Describe the morphology of the erythrocytes.
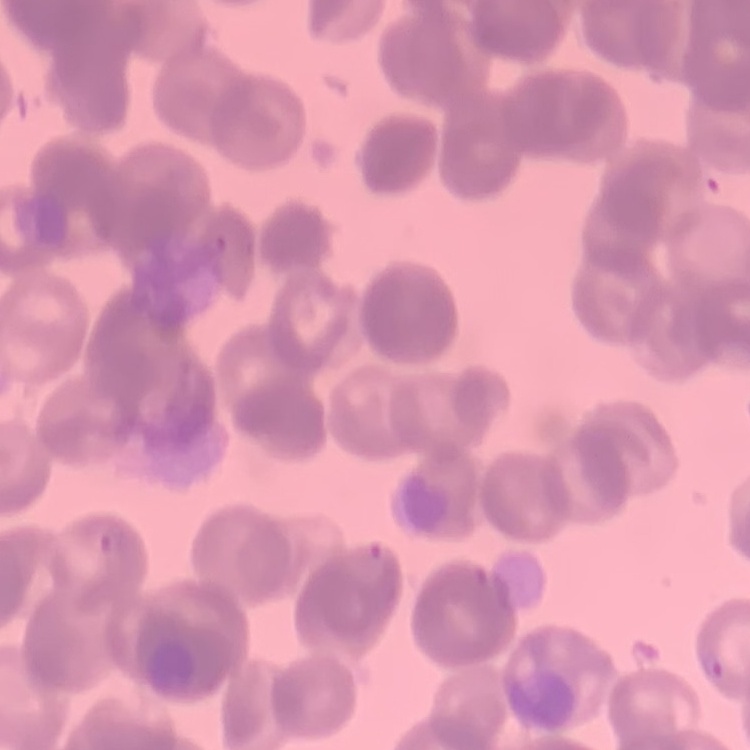
They show rouleaux formation.

Square crop of a larger photomicrograph. Thin blood film. Field's or Giemsa stain.